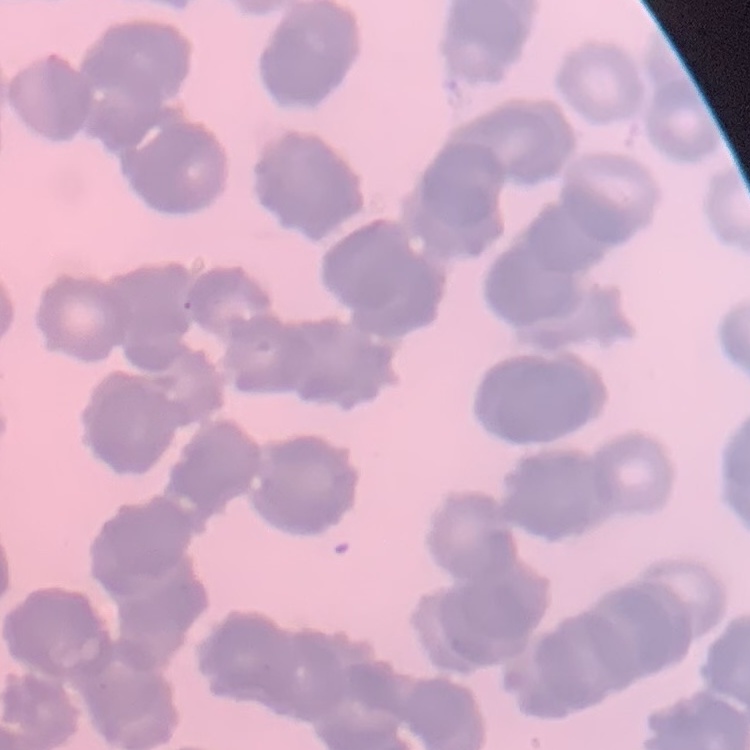
red_blood_cell_morphology: rouleaux formation
stain: Field's or Giemsa
preparation: thin blood smear
image_type: square crop of a larger photomicrograph